Give the extent of all Babesia divergens-infected red blood cells.
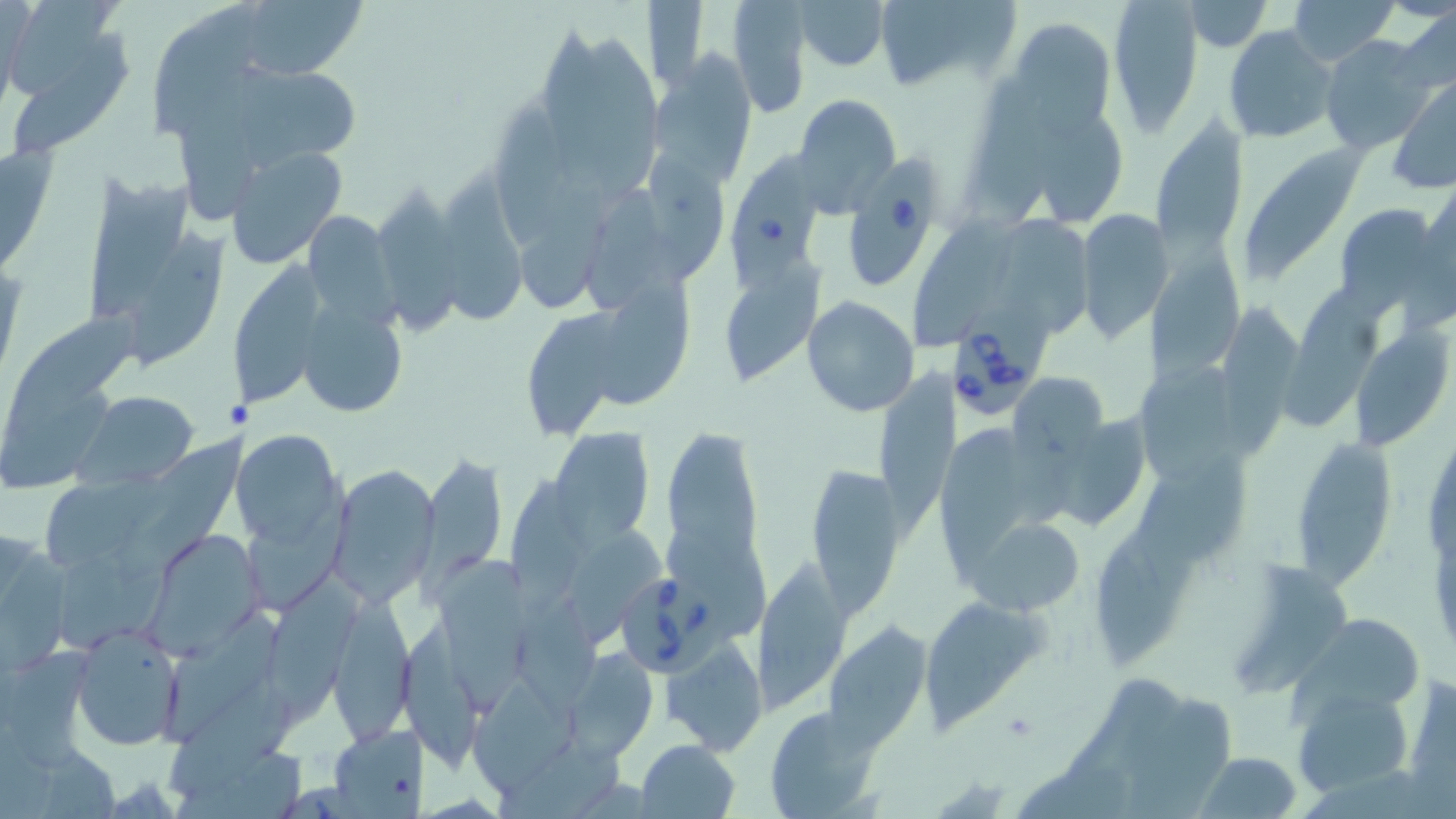
Approximate bounding boxes as (x1, y1, x2, y2) in pixels.
Babesia divergens-infected red blood cells: (726, 143, 818, 289), (847, 154, 939, 290), (948, 284, 1053, 420), (619, 565, 730, 683).

Summary:
  - Platelet locations: (1003, 711, 1039, 741)
  - Uninfected red blood cell locations: (9, 0, 121, 104), (726, 0, 811, 119), (795, 0, 889, 72), (873, 0, 1022, 94), (1106, 0, 1205, 138), (1288, 0, 1398, 64), (643, 1, 709, 91), (1185, 1, 1271, 50), (230, 2, 369, 82), (152, 3, 257, 138), (1396, 4, 1456, 96), (1009, 16, 1117, 130), (543, 23, 620, 185), (1224, 26, 1339, 145), (15, 28, 137, 161), (1320, 35, 1438, 155), (582, 36, 666, 191), (650, 50, 760, 188), (233, 66, 353, 170), (977, 72, 1064, 221), (1387, 78, 1456, 194), (179, 82, 255, 221), (793, 93, 902, 212), (493, 96, 564, 251), (1038, 111, 1123, 223), (1150, 118, 1247, 251), (0, 140, 56, 281), (1234, 143, 1364, 286), (223, 144, 350, 267), (646, 152, 726, 280), (85, 171, 201, 320), (517, 174, 615, 315), (435, 177, 534, 328), (374, 187, 467, 335), (585, 187, 661, 317), (1335, 199, 1446, 315), (306, 205, 414, 329), (1074, 209, 1171, 341), (917, 212, 1026, 349), (1009, 215, 1093, 336), (132, 229, 237, 368), (1142, 244, 1245, 397), (724, 255, 826, 385), (226, 268, 328, 410), (599, 273, 686, 410), (1281, 288, 1381, 432), (802, 295, 921, 418), (299, 298, 411, 416), (524, 305, 624, 442), (1218, 308, 1303, 461), (3, 312, 144, 439), (1352, 326, 1453, 448), (877, 366, 967, 533), (1136, 372, 1238, 485), (1010, 373, 1109, 462), (0, 391, 106, 492), (77, 391, 198, 486), (1066, 409, 1146, 526), (661, 419, 765, 597), (1285, 420, 1391, 593), (933, 421, 1030, 592), (551, 427, 654, 543), (124, 428, 251, 584), (235, 430, 345, 545), (1135, 445, 1250, 561), (418, 454, 507, 583), (331, 463, 437, 602), (805, 465, 906, 620), (44, 466, 160, 572), (511, 475, 583, 612), (243, 488, 362, 615), (967, 513, 1089, 617), (569, 524, 667, 648), (145, 527, 266, 658), (1093, 530, 1175, 667), (1, 533, 69, 676), (672, 537, 773, 636), (52, 543, 178, 650), (756, 553, 849, 710), (437, 555, 529, 706), (1232, 563, 1356, 695), (264, 572, 367, 715), (329, 593, 413, 742), (516, 593, 602, 724), (931, 596, 1052, 737), (1289, 614, 1421, 723), (404, 617, 497, 781), (167, 619, 291, 746), (824, 622, 932, 746), (72, 627, 183, 750), (664, 643, 768, 756), (6, 645, 98, 778), (564, 649, 660, 763), (472, 672, 574, 795), (162, 674, 299, 800), (1066, 676, 1191, 776), (1404, 677, 1456, 802), (1292, 687, 1415, 798), (1128, 694, 1232, 818), (763, 705, 882, 816), (326, 725, 427, 816), (636, 740, 741, 819), (498, 741, 623, 819), (174, 742, 308, 819), (40, 750, 116, 819), (1196, 752, 1303, 819), (1018, 765, 1133, 819)
  - Slide-level diagnosis: Babesia divergens
  - Magnification: 1000x
  - Preparation: thin blood film
  - Field of view: one of a larger specimen
  - Image size: 1456×819 pixels
  - Modality: optical microscopy
  - Stain: May-Grünwald-Giemsa